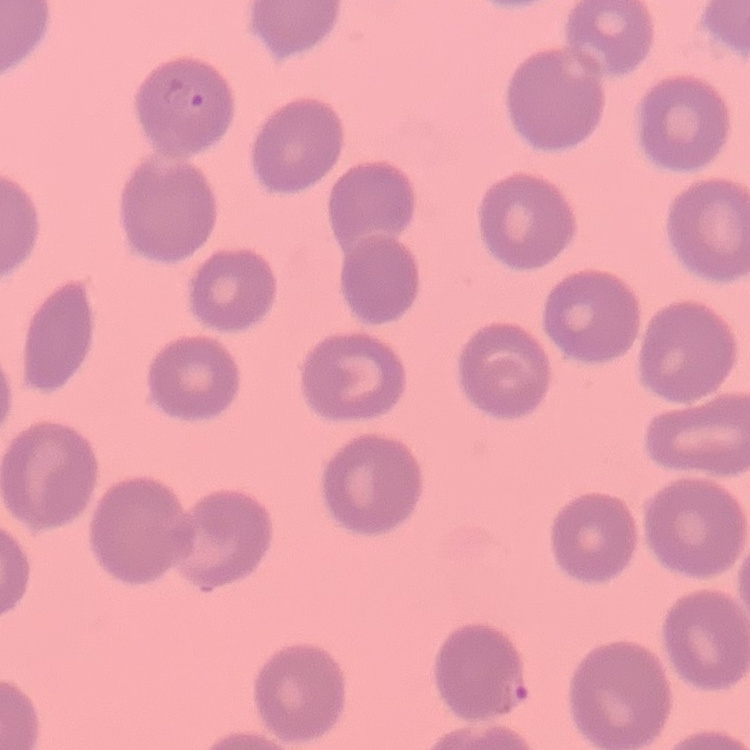
red blood cell morphology = no rouleaux formation
stain = Field's or Giemsa
image type = one tile cut from a larger photomicrograph
preparation = thin peripheral smear